State which parasite is depicted.
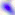
This is Toxoplasma gondii.

magnification = 400x
modality = photomicrograph